Outline each uninfected red blood cell.
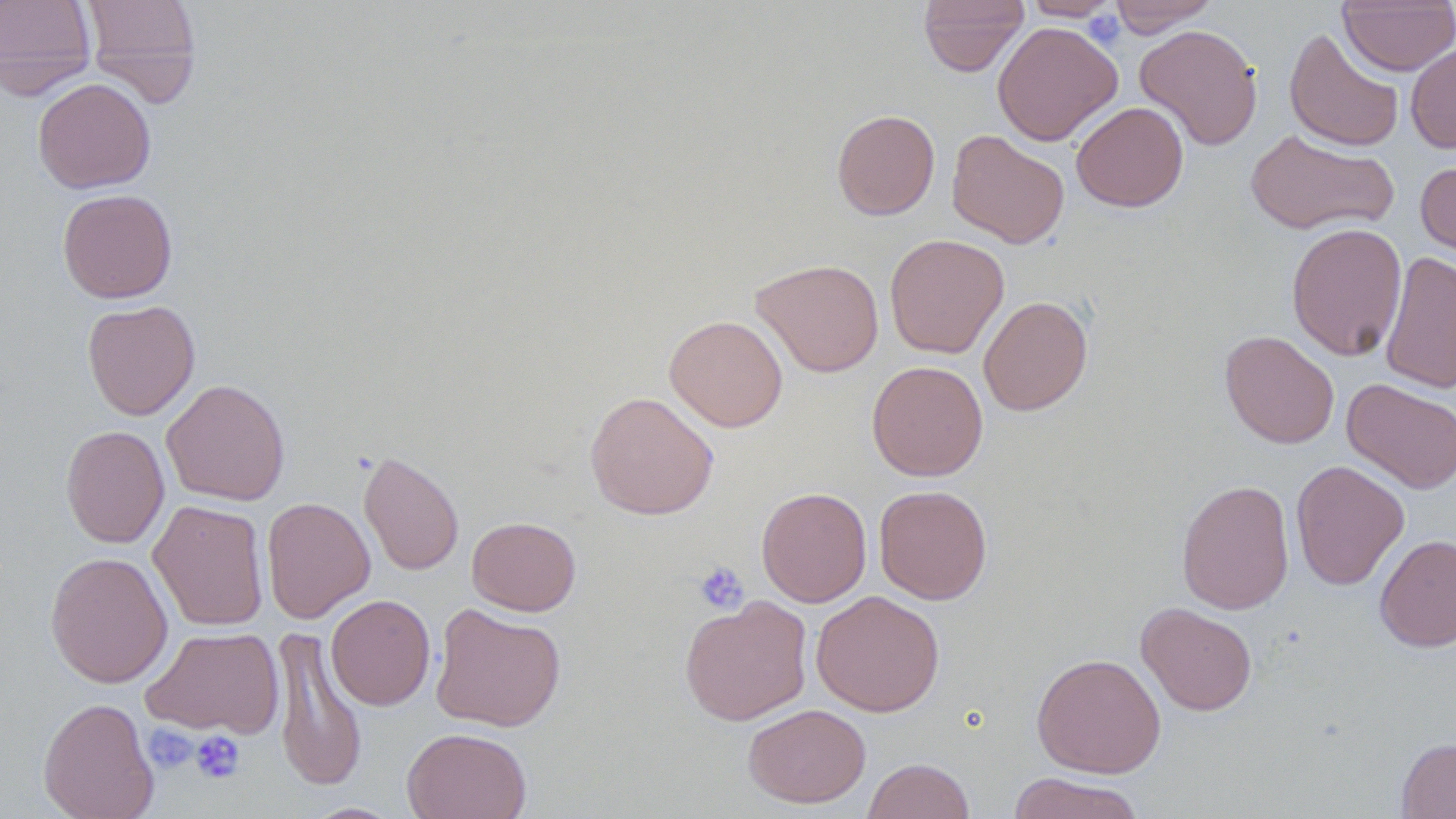

Approximate bounding boxes as (x1,y1)-(x2,y2) corner pairs in pixels.
Uninfected red blood cells: (0,0)-(97,99), (79,0)-(203,104), (918,0)-(1029,76), (1021,0)-(1123,21), (1108,0)-(1219,37), (1338,1)-(1456,75), (992,21)-(1122,146), (1134,23)-(1263,150), (1284,27)-(1405,152), (1406,43)-(1456,154), (33,77)-(156,194), (1071,101)-(1189,212), (831,109)-(940,220), (1245,128)-(1399,236), (947,129)-(1070,248), (1415,155)-(1456,268), (57,188)-(178,303), (1286,222)-(1407,361), (884,233)-(1009,359), (1380,251)-(1456,393), (751,258)-(884,377), (979,295)-(1093,416), (82,300)-(200,420), (664,314)-(788,432), (1220,330)-(1339,449), (867,360)-(988,481), (1342,378)-(1456,493), (161,379)-(291,506), (584,391)-(719,520), (60,424)-(169,548), (358,449)-(464,576), (1290,460)-(1410,590), (1175,479)-(1295,615), (874,485)-(992,604), (756,486)-(872,607), (260,496)-(375,624), (149,500)-(269,631), (466,516)-(581,615), (1374,534)-(1456,653), (45,551)-(173,688), (811,590)-(945,717), (326,594)-(436,710), (679,595)-(813,726), (1136,602)-(1258,716), (430,603)-(566,732), (271,625)-(368,792), (142,626)-(284,739), (1031,653)-(1166,777), (38,696)-(159,819), (743,703)-(871,807), (402,727)-(532,819), (1396,737)-(1456,818), (862,757)-(975,819), (1006,772)-(1146,819), (304,802)-(402,818).

Platelet locations: (1084,11)-(1126,49), (693,561)-(749,614), (143,724)-(198,773), (190,730)-(245,784). Slide-level diagnosis: no evidence of blood parasites. Optical microscopy. Captured at 1000x magnification. Thin blood film. Image is 1456×819 pixels. May-Grünwald-Giemsa-stained preparation. One field of a larger specimen.